Identify the blood parasite species.
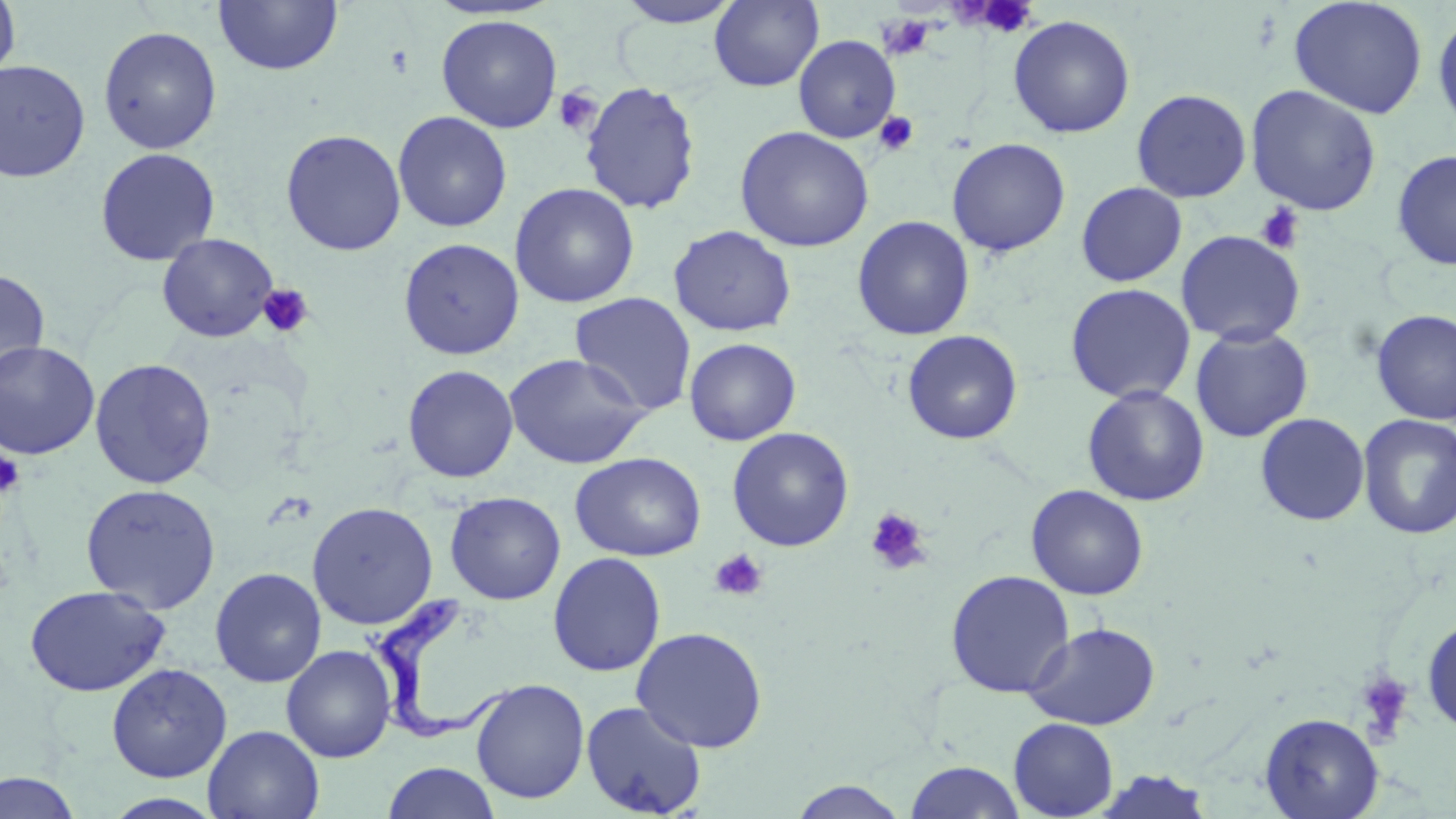

Trypanosoma brucei.

Summary:
  - Coordinate format: approximate bounding boxes as [x1, y1, x2, y2] in pixels
  - Trypanosoma brucei locations: [371, 587, 517, 742]
  - Uninfected red blood cell locations: [0, 0, 21, 86], [214, 0, 343, 76], [613, 0, 744, 28], [1289, 0, 1428, 120], [709, 1, 824, 91], [1432, 10, 1456, 137], [436, 14, 562, 133], [1007, 15, 1136, 138], [98, 25, 222, 154], [793, 34, 900, 143], [0, 60, 91, 182], [579, 81, 701, 215], [1245, 84, 1382, 215], [1131, 88, 1252, 202], [393, 111, 512, 232], [735, 126, 874, 252], [280, 129, 406, 256], [946, 138, 1070, 256], [94, 147, 220, 266], [1391, 150, 1456, 270], [510, 182, 639, 308], [1076, 182, 1187, 286], [852, 215, 975, 341], [668, 225, 796, 337], [1175, 230, 1305, 346], [157, 233, 278, 342], [398, 237, 524, 361], [0, 268, 50, 385], [1065, 283, 1196, 404], [569, 292, 697, 416], [1371, 308, 1456, 426], [1190, 326, 1313, 443], [902, 330, 1023, 445], [684, 337, 801, 446], [0, 340, 101, 460], [504, 353, 651, 469], [89, 358, 217, 489], [402, 364, 518, 483], [1082, 385, 1210, 506], [1255, 413, 1370, 526], [1357, 414, 1456, 540], [727, 427, 854, 551], [570, 452, 706, 561], [80, 483, 221, 614], [1026, 484, 1149, 600], [445, 491, 566, 605], [306, 501, 438, 630], [548, 552, 666, 677], [210, 567, 327, 688], [945, 570, 1075, 698], [24, 585, 171, 697], [1421, 616, 1456, 736], [1024, 622, 1160, 730], [631, 626, 768, 753], [281, 644, 397, 762], [106, 663, 232, 782], [470, 678, 590, 804], [580, 700, 707, 818], [1260, 712, 1384, 819], [1008, 718, 1118, 818], [203, 725, 324, 818], [903, 761, 1027, 818], [382, 762, 501, 819], [1090, 769, 1216, 819], [0, 770, 81, 819], [785, 779, 912, 818], [103, 792, 225, 818]
  - Platelet locations: [980, 1, 1037, 35], [553, 86, 602, 136], [874, 112, 919, 155], [1255, 203, 1305, 254], [257, 283, 314, 338], [0, 449, 24, 499], [865, 507, 932, 575], [709, 548, 768, 602], [1355, 671, 1415, 742]
  - Preparation: thin blood smear
  - Field of view: single
  - Stain: May-Grünwald-Giemsa
  - Magnification: 1000x
  - Image size: 1456×819 pixels
  - Modality: light microscopy